Locate every uninfected red blood cell.
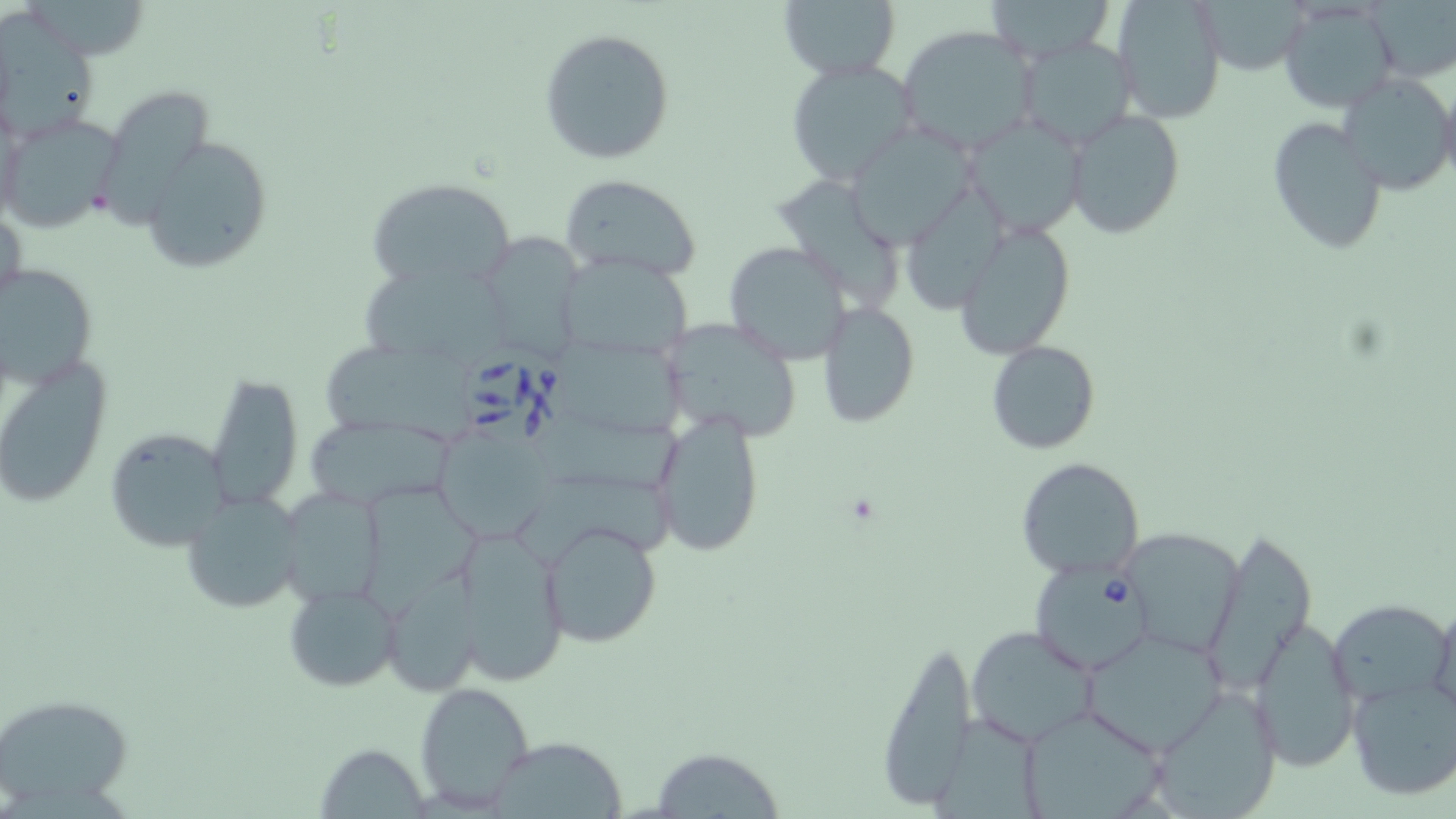
Approximate bounding boxes as (x1,y1)-(x2,y2) corner pairs in pixels.
Uninfected red blood cells: (777,0)-(901,83), (981,0)-(1115,64), (1112,0)-(1227,124), (1194,0)-(1315,76), (1370,1)-(1456,82), (1276,2)-(1399,112), (0,9)-(103,145), (896,25)-(1040,158), (539,27)-(675,164), (1014,35)-(1139,153), (785,59)-(918,187), (1337,71)-(1456,198), (1437,83)-(1456,192), (98,98)-(222,226), (1063,110)-(1186,240), (2,112)-(119,233), (963,114)-(1088,238), (1266,116)-(1389,254), (844,122)-(981,247), (142,137)-(271,273), (559,174)-(703,282), (781,176)-(897,310), (366,177)-(514,293), (907,186)-(1008,308), (1,203)-(27,321), (954,218)-(1077,356), (475,231)-(590,363), (723,240)-(853,365), (560,255)-(693,364), (0,260)-(100,391), (357,266)-(513,367), (817,303)-(920,427), (660,317)-(806,444), (554,335)-(698,442), (321,339)-(486,444), (986,340)-(1100,455), (0,357)-(113,510), (204,371)-(306,511), (650,408)-(765,558), (527,415)-(688,493), (304,419)-(456,509), (433,426)-(556,545), (104,430)-(228,550), (1015,456)-(1146,581), (522,473)-(690,565), (369,485)-(485,612), (276,487)-(387,606), (181,490)-(306,615), (540,519)-(665,648), (449,524)-(572,686), (1118,526)-(1244,659), (1209,528)-(1317,691), (381,575)-(484,699), (283,582)-(402,693), (1429,596)-(1456,719), (1329,597)-(1450,709), (1247,615)-(1360,773), (966,625)-(1099,749), (1080,628)-(1229,753), (874,639)-(977,812), (1345,675)-(1456,802), (413,681)-(536,813), (1148,686)-(1283,818), (0,692)-(134,812), (1015,705)-(1172,819), (931,713)-(1046,819), (489,735)-(628,819), (313,741)-(433,816), (650,745)-(786,817).

Summary:
  - Babesia divergens-infected red blood cell locations: (459,345)-(579,454), (1029,561)-(1149,675)
  - Slide-level diagnosis: Babesia divergens
  - Modality: optical microscopy
  - Field of view: one of a larger specimen
  - Preparation: thin blood film
  - Image size: 1456×819 pixels
  - Magnification: 1000x
  - Stain: May-Grünwald-Giemsa